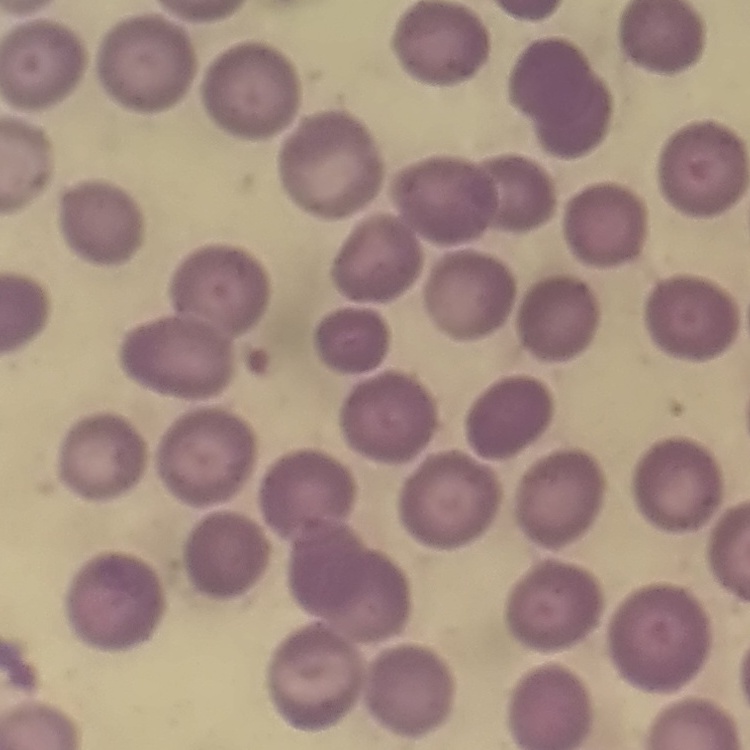

Summary:
  - Red blood cell morphology: no rouleaux formation
  - Image type: square crop of a larger photomicrograph
  - Stain: Field's or Giemsa
  - Preparation: thin peripheral smear